Report the malaria status of this cell.
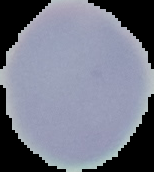
Uninfected.

Image is 154×172 pixels. From a thin blood smear. Cell region segmented out of the field of view; the surrounding area is masked to black.